Locate and identify every blood parasite.
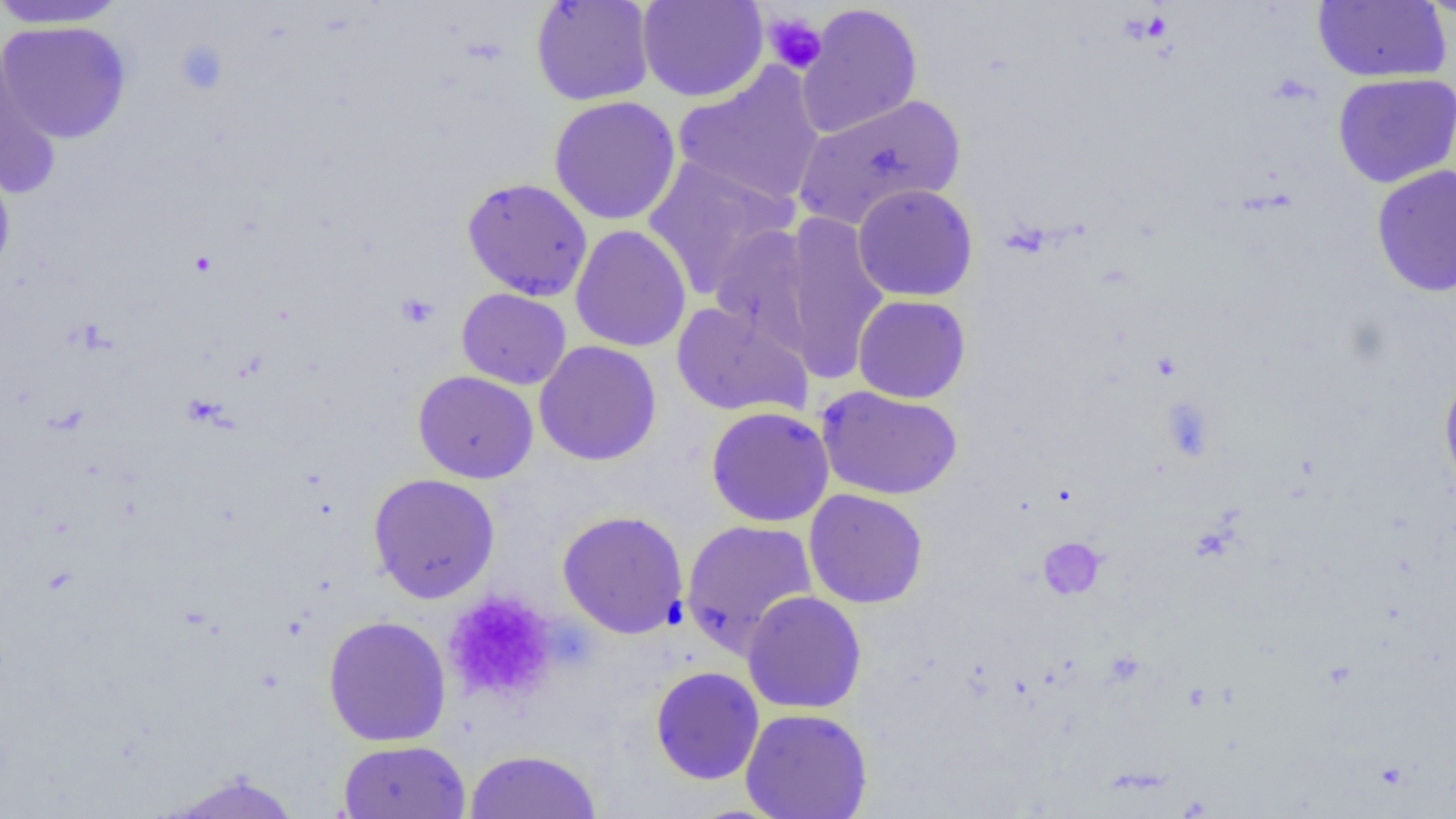

No blood parasites seen.

slide-level diagnosis = negative for blood parasites
platelet locations = approximate bounding boxes as (x1,y1)-(x2,y2) corner pairs in pixels: (762,13)-(827,75), (173,39)-(230,96), (396,292)-(439,329), (1160,396)-(1216,461), (1038,537)-(1105,600), (442,589)-(557,705)
magnification = 1000x
field of view = one of a larger specimen
preparation = thin blood film
uninfected red blood cell locations = approximate bounding boxes as (x1,y1)-(x2,y2) corner pairs in pixels: (530,0)-(656,106), (637,0)-(769,102), (1416,0)-(1455,22), (0,1)-(130,29), (1312,1)-(1451,83), (797,3)-(923,138), (1,20)-(132,143), (0,45)-(61,196), (673,63)-(826,209), (1332,73)-(1456,188), (794,92)-(966,230), (549,96)-(681,225), (0,152)-(16,286), (642,157)-(797,298), (1371,164)-(1456,298), (461,177)-(593,302), (852,183)-(978,302), (780,212)-(890,382), (708,223)-(817,352), (570,224)-(691,352), (456,288)-(571,390), (853,294)-(971,403), (671,301)-(811,418), (534,341)-(662,466), (413,370)-(538,483), (1439,370)-(1456,500), (817,385)-(962,500), (705,406)-(834,526), (368,473)-(500,604), (803,488)-(928,609), (557,509)-(689,638), (681,519)-(818,656), (742,590)-(867,714), (322,615)-(452,747), (650,666)-(764,785), (740,708)-(873,819), (337,739)-(471,818), (463,749)-(601,818), (157,771)-(307,818)
image size = 1456×819 pixels
modality = light microscopy